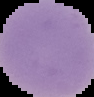

image_type: segmented cell region with the area outside set to black
malaria_status: uninfected
preparation: thin blood smear
image_size: 94×97 pixels